State the blood parasite species.
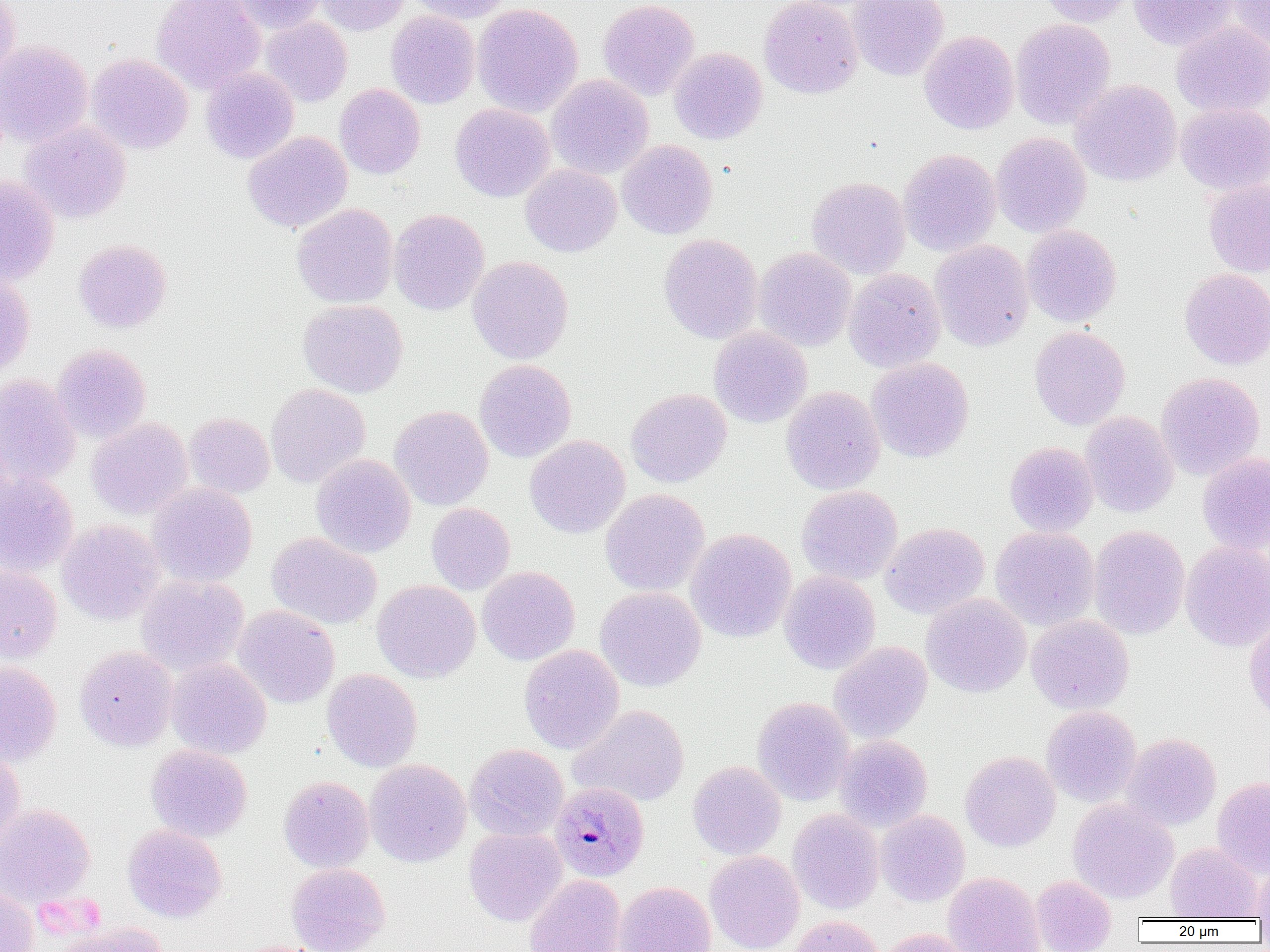

Plasmodium malariae.

uninfected red blood cell locations = approximate bounding boxes as (x1, y1, x2, y2) in pixels: (0, 0, 21, 86), (151, 0, 265, 95), (232, 0, 327, 34), (313, 0, 410, 35), (405, 0, 515, 23), (598, 0, 699, 100), (759, 0, 863, 99), (848, 0, 950, 80), (1038, 0, 1135, 27), (1128, 0, 1235, 51), (1224, 0, 1270, 51), (472, 3, 583, 117), (385, 10, 480, 109), (260, 17, 352, 107), (1010, 18, 1115, 130), (1171, 21, 1270, 118), (919, 30, 1019, 134), (0, 40, 93, 147), (669, 47, 768, 144), (86, 53, 194, 154), (201, 67, 299, 164), (546, 74, 654, 180), (1070, 79, 1182, 186), (335, 84, 425, 179), (1176, 102, 1269, 196), (450, 103, 555, 202), (20, 120, 132, 223), (243, 131, 353, 234), (991, 132, 1091, 237), (618, 140, 718, 239), (898, 148, 1000, 257), (520, 164, 621, 257), (0, 174, 60, 285), (806, 176, 911, 279), (1203, 179, 1270, 277), (292, 203, 399, 308), (389, 209, 489, 315), (1021, 224, 1121, 327), (658, 233, 763, 344), (73, 239, 172, 333), (930, 239, 1033, 352), (754, 247, 856, 351), (467, 256, 573, 364), (844, 268, 946, 373), (1179, 268, 1270, 370), (0, 273, 35, 379), (298, 300, 408, 398), (1029, 326, 1130, 429), (709, 327, 812, 428), (52, 344, 152, 443), (867, 357, 974, 462), (475, 359, 576, 463), (1156, 372, 1265, 480), (0, 375, 81, 487), (266, 383, 371, 488), (781, 385, 884, 495), (626, 388, 732, 488), (390, 405, 494, 511), (1080, 411, 1178, 518), (184, 412, 275, 498), (86, 417, 193, 520), (525, 435, 630, 538), (1004, 441, 1099, 537), (1197, 452, 1270, 554), (311, 454, 416, 558), (0, 469, 79, 577), (147, 483, 257, 587), (796, 485, 902, 585), (600, 488, 710, 596), (426, 503, 515, 595), (56, 519, 165, 625), (880, 522, 990, 619), (1088, 525, 1190, 639), (990, 526, 1100, 630), (686, 528, 796, 642), (266, 532, 382, 629), (1180, 540, 1270, 652), (0, 564, 62, 662), (477, 566, 579, 665), (779, 570, 881, 674), (136, 575, 249, 676), (372, 580, 480, 682), (595, 587, 706, 692), (921, 593, 1031, 697), (232, 605, 340, 708), (1244, 608, 1270, 725), (1026, 614, 1134, 714), (829, 641, 932, 742), (519, 644, 624, 755), (75, 646, 177, 751), (165, 657, 272, 759), (0, 661, 62, 766), (322, 668, 422, 772), (752, 696, 855, 806), (569, 704, 690, 806), (1040, 706, 1142, 807), (1122, 733, 1221, 830), (834, 735, 932, 833), (145, 744, 252, 842), (465, 744, 568, 841), (0, 748, 26, 848), (960, 751, 1060, 851), (365, 759, 471, 868), (687, 761, 786, 860), (279, 776, 374, 873), (1212, 777, 1270, 877), (1068, 799, 1179, 903), (0, 803, 95, 906), (787, 809, 884, 915), (876, 810, 970, 907), (122, 824, 227, 923), (464, 827, 566, 926), (1165, 842, 1262, 920), (704, 850, 804, 952), (286, 863, 390, 952), (1252, 863, 1270, 920), (942, 872, 1045, 952), (525, 875, 626, 952), (1031, 875, 1116, 952), (614, 881, 716, 952), (0, 884, 39, 952), (788, 915, 884, 952), (53, 922, 170, 952), (874, 928, 974, 952)
preparation = thin blood film
modality = light microscopy
Plasmodium malariae-infected red blood cell locations = approximate bounding boxes as (x1, y1, x2, y2) in pixels: (551, 781, 649, 881)
image size = 1270×952 pixels
magnification = 1000x
field of view = one of a larger specimen